State which cell type is depicted.
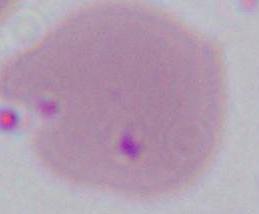

An erythrocyte.

Summary:
  - Modality: photomicrograph
  - Magnification: 1000x